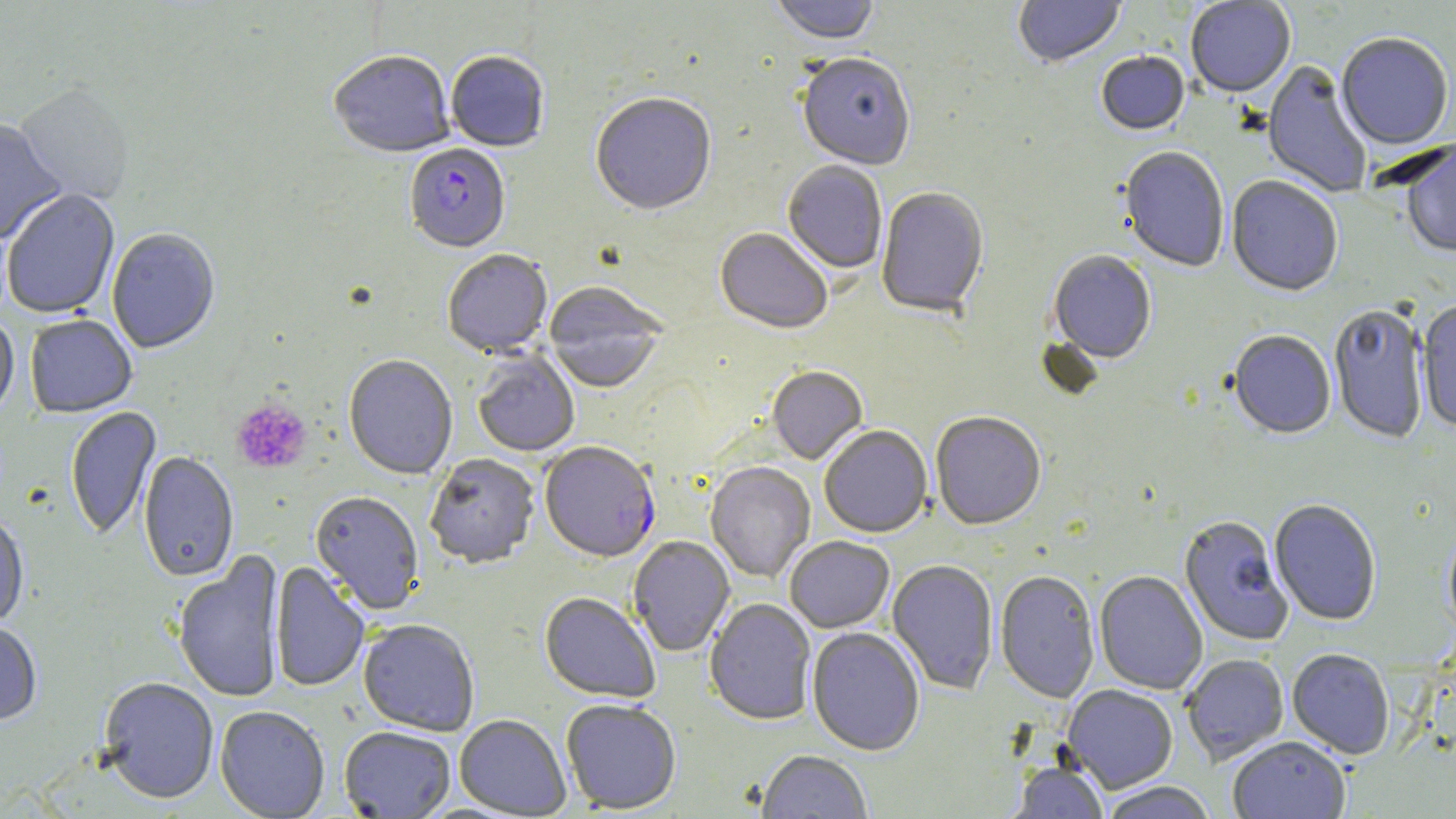

{
  "slide_level_diagnosis": "Plasmodium falciparum",
  "stain": "May-Grünwald-Giemsa",
  "magnification": "1000x",
  "modality": "light microscopy",
  "platelet_locations": "approximate bounding boxes as [x1, y1, x2, y2] in pixels: [231, 398, 312, 475]",
  "preparation": "thin blood smear",
  "uninfected_red_blood_cell_locations": "approximate bounding boxes as [x1, y1, x2, y2] in pixels: [770, 0, 880, 47], [1014, 0, 1126, 68], [1186, 1, 1295, 99], [1336, 35, 1454, 152], [329, 53, 454, 160], [446, 53, 550, 153], [1096, 53, 1189, 137], [797, 55, 915, 173], [1262, 61, 1372, 198], [14, 87, 134, 206], [591, 95, 717, 219], [0, 120, 67, 247], [1401, 142, 1456, 260], [1118, 148, 1230, 273], [782, 162, 887, 275], [1226, 178, 1343, 298], [876, 188, 989, 320], [2, 190, 121, 320], [715, 229, 832, 336], [107, 230, 220, 355], [442, 252, 553, 359], [1047, 252, 1156, 365], [543, 283, 668, 395], [1417, 301, 1456, 433], [1329, 307, 1429, 445], [25, 316, 137, 419], [0, 318, 19, 423], [1228, 332, 1335, 440], [472, 351, 580, 458], [343, 356, 458, 481], [767, 367, 868, 465], [65, 407, 162, 541], [931, 413, 1046, 531], [819, 426, 933, 539], [137, 452, 239, 584], [425, 455, 540, 570], [705, 462, 815, 583], [310, 492, 424, 616], [1269, 500, 1381, 626], [0, 515, 29, 631], [1179, 516, 1294, 646], [1443, 523, 1456, 640], [628, 536, 736, 657], [785, 536, 895, 634], [172, 550, 286, 705], [886, 560, 999, 695], [270, 562, 369, 693], [1094, 570, 1208, 696], [995, 571, 1100, 703], [539, 593, 661, 705], [704, 599, 817, 726], [358, 621, 479, 737], [0, 623, 42, 727], [806, 628, 925, 757], [1287, 649, 1395, 760], [1182, 654, 1289, 765], [98, 678, 219, 805], [1063, 685, 1177, 793], [561, 700, 681, 814], [214, 707, 330, 818], [454, 715, 570, 818], [339, 728, 456, 818], [1228, 738, 1350, 819], [757, 751, 873, 819], [1009, 762, 1108, 819], [1098, 782, 1218, 819]",
  "image_size": "1456×819 pixels",
  "field_of_view": "one of a larger specimen",
  "plasmodium_falciparum_infected_red_blood_cell_locations": "approximate bounding boxes as [x1, y1, x2, y2] in pixels: [405, 145, 510, 255], [540, 443, 660, 564]"
}